Identify the parasite.
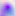

Toxoplasma gondii.

Captured at 400x magnification. Photomicrograph.